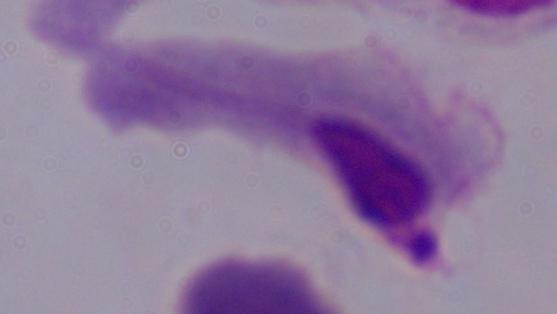

1000x magnification. A trichomonad is seen. Photomicrograph.